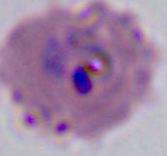

Micrograph. 400x or 1000x magnification. A Plasmodium parasite is seen.